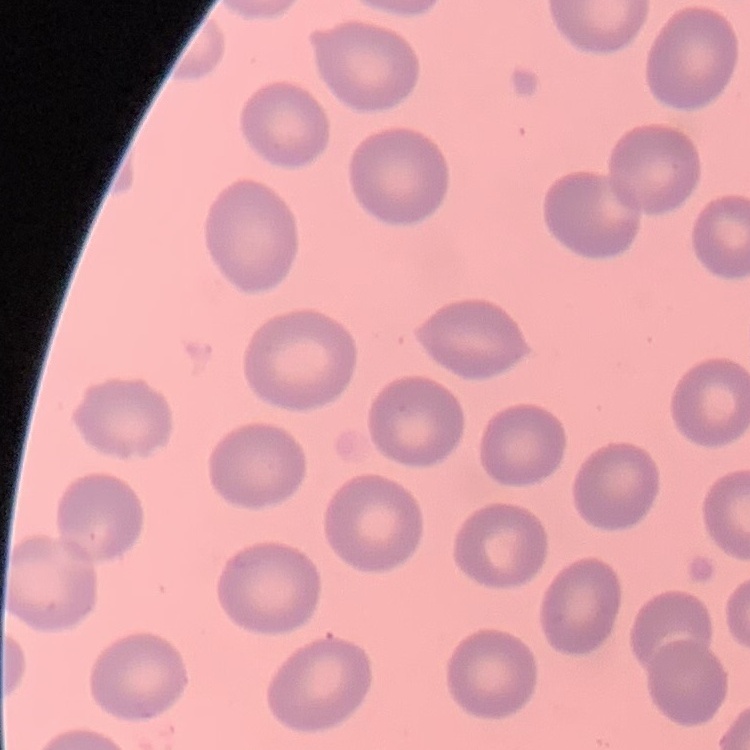
red blood cell morphology = no rouleaux formation
image type = square crop of a larger photomicrograph
preparation = thin blood smear
stain = Field's or Giemsa